Identify the parasite.
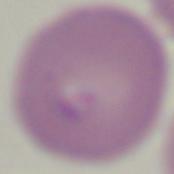
This is Babesia.

Photomicrograph. 1000x magnification.